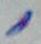
Captured at 1000x magnification. Toxoplasma gondii is seen. Micrograph.